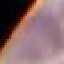

Malaria status: uninfected. Thin blood film. Cell patch, automatically extracted from a larger field of view and resized to 64 × 64 pixels. Giemsa-stained preparation. Photographed with a smartphone camera at the microscope eyepiece.